Report the malaria status.
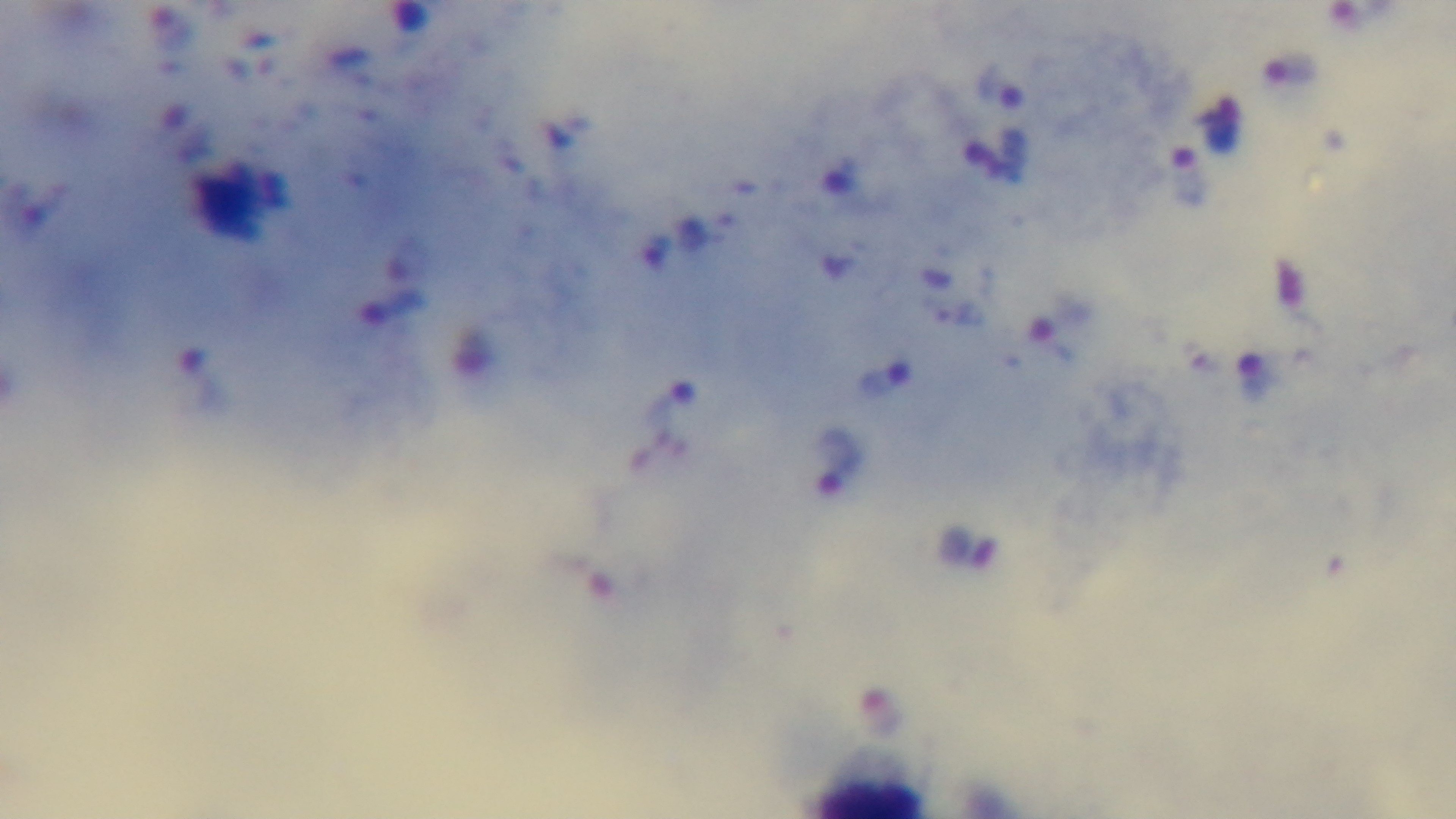
Positive.

Summary:
  - Field of view: single
  - Modality: light microscopy
  - Stain: Giemsa
  - Preparation: thick
  - Capture: mounted 4K digital camera
  - Objective: 100x oil immersion